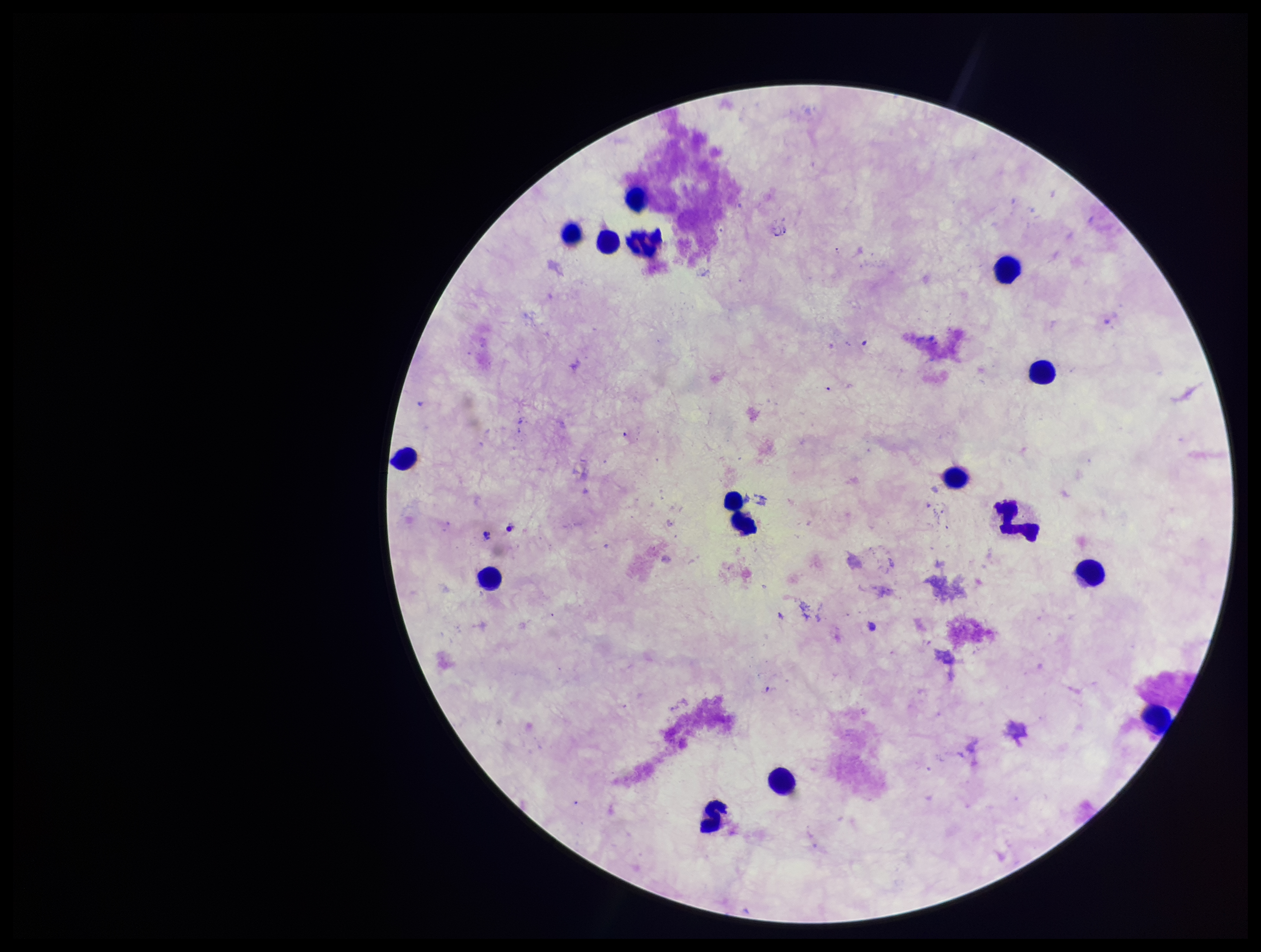

capture = smartphone photograph through the microscope eyepiece
Plasmodium parasites = none identified
parasite count = 0
leukocyte count = 16
image size = 1261×952 pixels
preparation = thick blood smear
patient malaria status = negative
stain = Giemsa
field of view = single